Outline each Plasmodium falciparum-infected red blood cell.
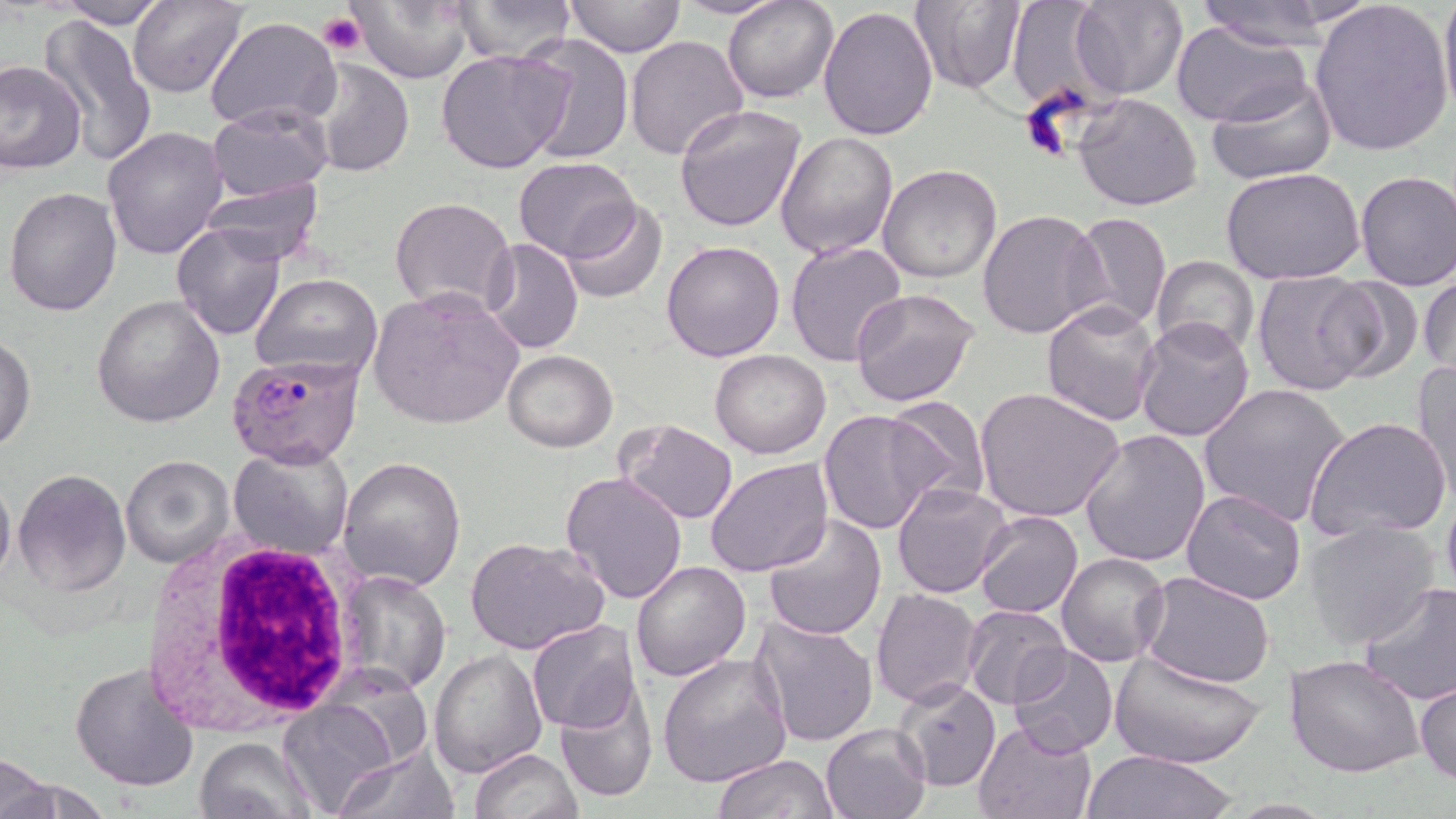
Approximate bounding boxes as [x1, y1, x2, y2] in pixels.
Plasmodium falciparum-infected red blood cells: [228, 354, 365, 469].

Platelet locations: [318, 11, 366, 55], [1018, 99, 1079, 163]. Uninfected red blood cell locations: [129, 0, 250, 99], [347, 0, 475, 85], [450, 0, 578, 63], [669, 0, 792, 19], [723, 0, 838, 102], [910, 0, 1028, 93], [1070, 0, 1186, 100], [1192, 0, 1344, 50], [1438, 0, 1456, 121], [58, 1, 173, 29], [563, 1, 686, 58], [1004, 1, 1114, 112], [1308, 3, 1454, 158], [818, 5, 939, 141], [38, 16, 158, 164], [204, 16, 341, 134], [1171, 20, 1314, 129], [521, 33, 633, 164], [626, 34, 748, 159], [436, 48, 573, 175], [302, 55, 415, 177], [0, 61, 85, 173], [1206, 75, 1338, 185], [1072, 92, 1204, 210], [207, 104, 334, 202], [675, 105, 807, 232], [103, 126, 228, 259], [774, 130, 898, 260], [513, 156, 642, 261], [878, 163, 1002, 283], [1219, 167, 1367, 285], [1355, 170, 1456, 292], [197, 175, 326, 264], [4, 187, 123, 315], [390, 196, 516, 317], [561, 199, 667, 305], [978, 208, 1107, 341], [1066, 212, 1172, 335], [171, 220, 285, 340], [481, 240, 584, 355], [660, 241, 785, 363], [786, 241, 908, 367], [1151, 256, 1260, 360], [1420, 266, 1455, 380], [1251, 270, 1378, 396], [251, 272, 382, 381], [1313, 275, 1420, 385], [848, 287, 982, 407], [368, 288, 524, 429], [90, 293, 226, 429], [1040, 302, 1163, 427], [1132, 317, 1257, 443], [0, 335, 36, 456], [502, 349, 617, 453], [709, 349, 831, 459], [1413, 359, 1456, 494], [1197, 382, 1351, 528], [974, 386, 1127, 524], [881, 396, 990, 507], [819, 409, 945, 536], [1305, 415, 1452, 544], [617, 419, 738, 524], [1080, 429, 1210, 567], [229, 443, 355, 560], [120, 453, 235, 570], [337, 455, 467, 591], [705, 457, 834, 577], [12, 468, 132, 597], [0, 471, 14, 592], [560, 472, 688, 607], [891, 483, 1015, 600], [1440, 483, 1456, 606], [1181, 490, 1308, 606], [975, 510, 1083, 617], [762, 514, 888, 641], [1305, 518, 1441, 649], [465, 536, 610, 656], [1055, 551, 1170, 668], [629, 560, 751, 682], [340, 569, 452, 695], [1139, 572, 1279, 691], [1359, 582, 1456, 705], [870, 588, 985, 709], [961, 604, 1070, 710], [750, 616, 880, 749], [525, 619, 642, 735], [1008, 645, 1119, 758], [428, 646, 547, 777], [1111, 651, 1265, 770], [657, 652, 792, 789], [1284, 652, 1425, 776], [69, 660, 200, 793], [322, 668, 436, 768], [893, 672, 1002, 794], [1415, 677, 1456, 785], [553, 681, 659, 802], [276, 700, 398, 818], [973, 720, 1096, 819], [820, 722, 932, 819], [193, 736, 317, 819], [331, 746, 461, 819], [468, 747, 581, 819], [1078, 749, 1237, 818], [0, 752, 58, 819], [713, 754, 839, 818]. White blood cell locations: [137, 533, 366, 732]. Slide-level diagnosis: Plasmodium falciparum. Optical microscopy. May-Grünwald-Giemsa-stained preparation. One field of a larger specimen. 1000x magnification. Thin blood film. Image is 1456×819 pixels.